Describe the morphology of the erythrocytes.
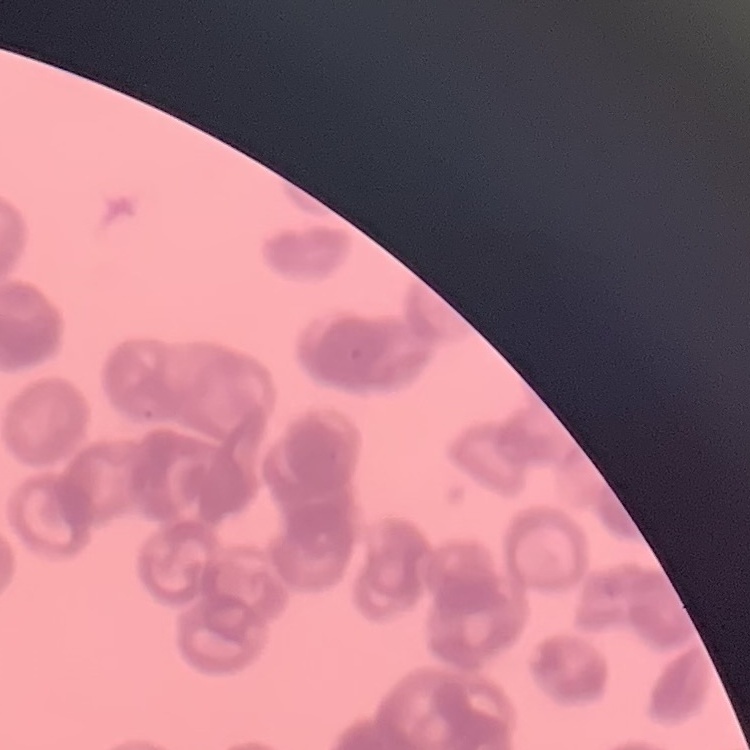

They show rouleaux formation.

Summary:
  - Stain: Field's or Giemsa
  - Image type: square crop of a larger photomicrograph
  - Preparation: thin peripheral smear